Assess this cell for malaria.
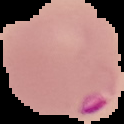
Parasitized.

Image is 124×124 pixels. From a thin blood film. Cell region segmented out of the field of view; the surrounding area is masked to black.